Classify this cell by malaria status.
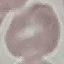

Uninfected.

stain: Giemsa
image_type: automatically extracted cell patch, resized to 64 × 64 pixels
capture: smartphone through the microscope eyepiece
preparation: thin smear